Outline each Plasmodium vivax-infected red blood cell.
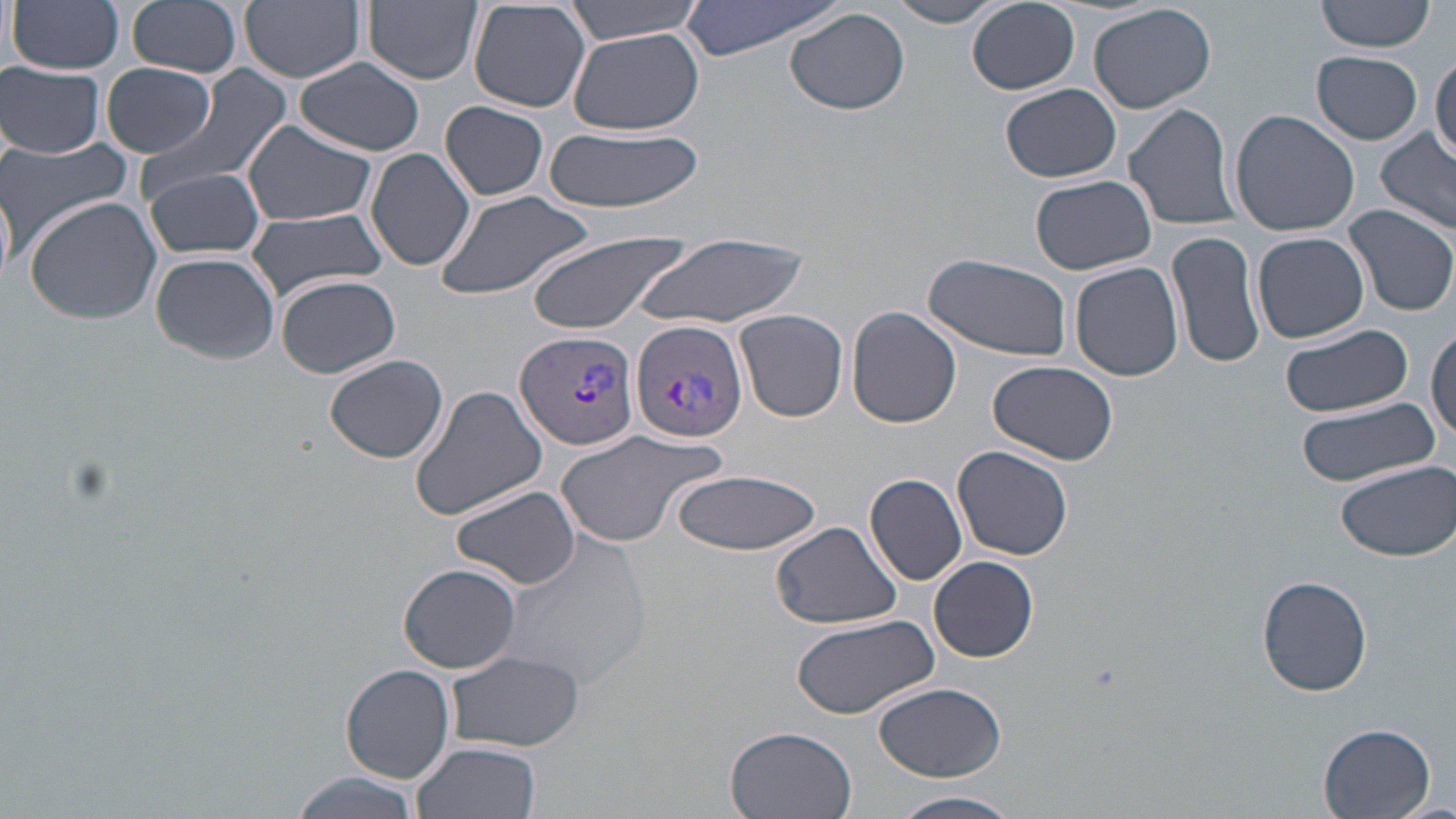
Approximate bounding boxes as [x1, y1, x2, y2] in pixels.
Plasmodium vivax-infected red blood cells: [630, 319, 748, 444], [515, 328, 641, 452].

slide-level diagnosis = Plasmodium vivax
uninfected red blood cell locations = approximate bounding boxes as [x1, y1, x2, y2] in pixels: [8, 0, 125, 74], [127, 0, 242, 78], [240, 0, 366, 83], [364, 0, 481, 86], [563, 0, 704, 45], [678, 0, 848, 60], [886, 0, 1012, 27], [1317, 0, 1437, 53], [468, 1, 594, 114], [967, 1, 1079, 94], [1089, 3, 1218, 113], [785, 7, 911, 115], [569, 29, 704, 135], [1312, 51, 1423, 144], [1431, 52, 1455, 164], [295, 58, 425, 156], [0, 61, 106, 158], [101, 62, 219, 159], [144, 64, 294, 199], [1001, 85, 1121, 183], [440, 101, 550, 200], [1122, 101, 1241, 231], [1229, 109, 1360, 235], [244, 120, 376, 226], [544, 125, 704, 214], [1376, 130, 1456, 234], [0, 137, 136, 249], [366, 147, 477, 272], [144, 166, 266, 259], [1029, 174, 1156, 274], [0, 177, 15, 293], [433, 189, 596, 301], [22, 194, 166, 324], [1344, 206, 1456, 316], [245, 210, 392, 301], [526, 229, 694, 335], [633, 230, 810, 331], [1169, 230, 1266, 370], [1252, 232, 1370, 344], [150, 251, 280, 364], [924, 254, 1073, 362], [1070, 262, 1184, 383], [276, 274, 402, 378], [847, 306, 961, 428], [734, 309, 847, 421], [1279, 324, 1413, 418], [1428, 325, 1456, 442], [325, 355, 449, 464], [987, 360, 1118, 464], [410, 384, 552, 521], [1296, 400, 1442, 488], [554, 426, 730, 549], [953, 446, 1073, 562], [1334, 460, 1456, 562], [667, 470, 822, 553], [865, 474, 969, 585], [451, 485, 584, 592], [770, 521, 903, 630], [498, 531, 652, 694], [929, 556, 1038, 662], [399, 563, 522, 673], [1255, 574, 1373, 696], [791, 612, 941, 719], [444, 649, 587, 751], [341, 663, 456, 784], [872, 682, 1007, 781], [1318, 723, 1437, 818], [724, 726, 858, 819], [410, 742, 542, 819], [287, 774, 419, 819], [890, 791, 1026, 819]
modality = optical microscopy
field of view = one of a larger specimen
stain = May-Grünwald-Giemsa
image size = 1456×819 pixels
magnification = 1000x
preparation = thin blood film